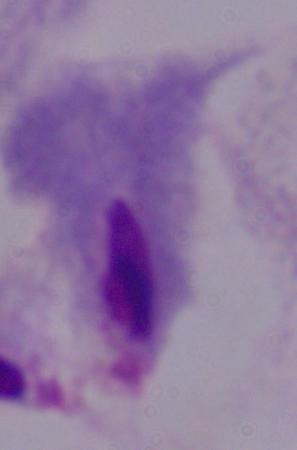

identification: trichomonad
magnification: 1000x
modality: photomicrograph